Locate every Plasmodium parasite.
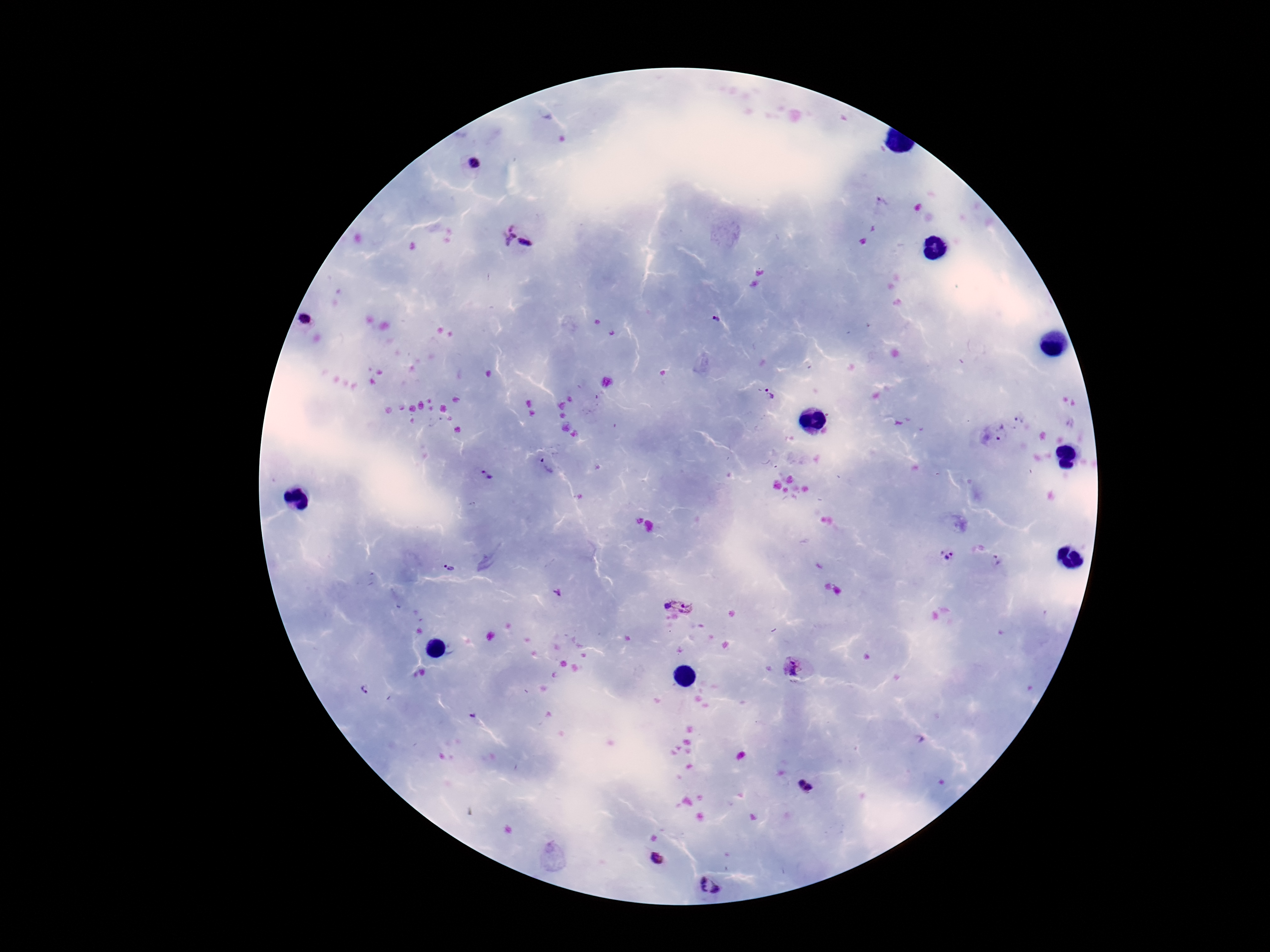

Approximate centers as [x, y] in pixels.
Plasmodium parasites: [473, 162], [881, 204], [504, 235], [526, 242], [717, 319], [308, 320], [771, 394], [1020, 417], [1002, 433], [546, 468], [485, 475], [950, 554], [999, 561], [451, 568], [558, 593], [677, 604], [791, 666], [366, 689], [472, 716], [802, 783], [808, 788], [551, 851], [657, 858], [710, 886].

Smartphone photograph taken through the microscope eyepiece. Patient malaria status: positive. Giemsa stain. 100x magnification. Thick blood smear. Image is 1270×952 pixels. Single field of view.